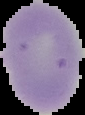
Summary:
  - Preparation: thin blood film
  - Image size: 85×115 pixels
  - Image type: cell region segmented out of the field of view; surrounding area masked to black
  - Result: no Plasmodium parasites seen